Locate and identify every blood parasite.
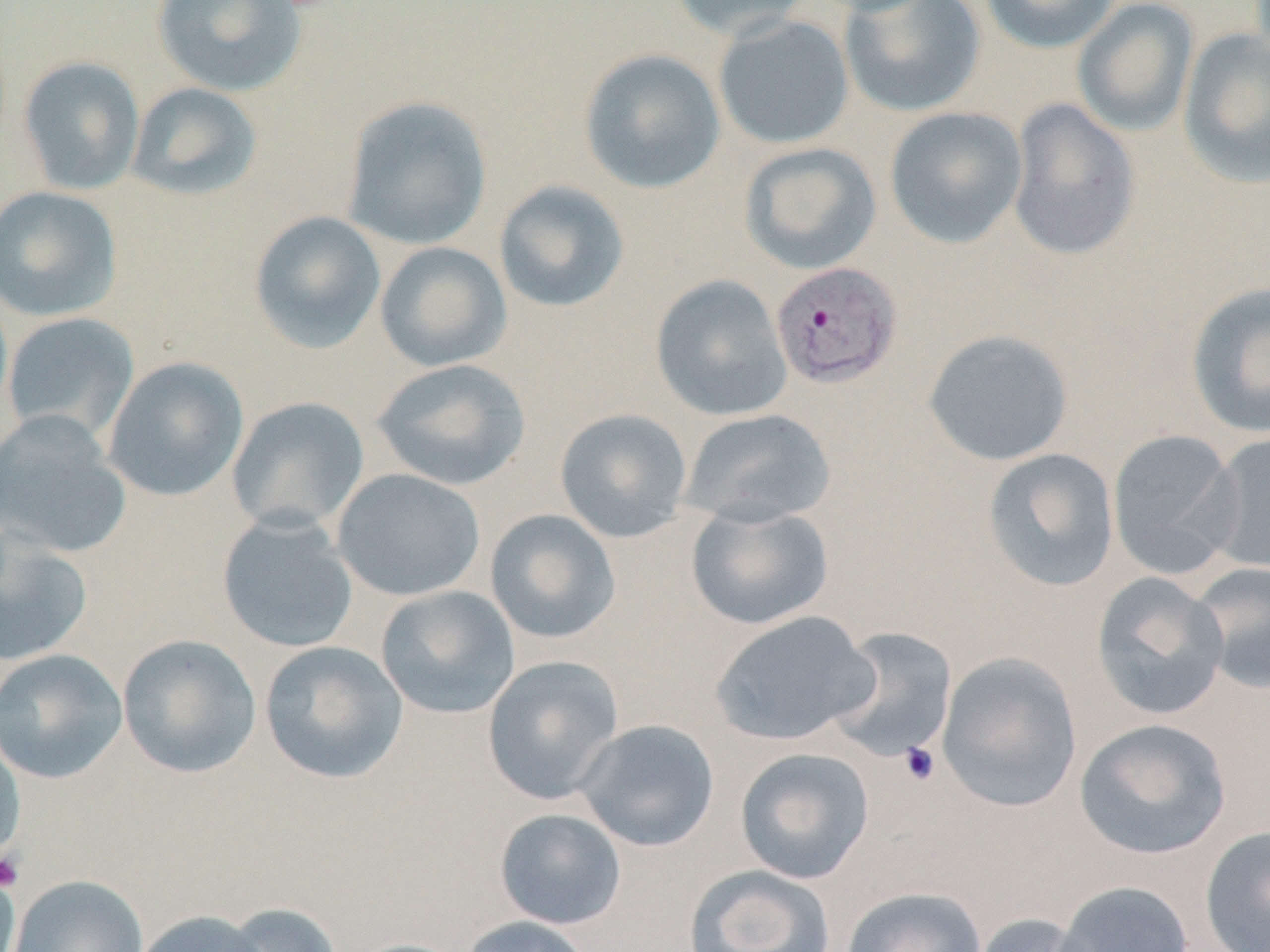

Approximate bounding boxes as (x1, y1, x2, y2) in pixels.
Plasmodium vivax-infected red blood cells: (769, 261, 903, 389).
No Plasmodium falciparum, Plasmodium ovale, Plasmodium malariae, Babesia divergens, or Trypanosoma brucei observed.

Summary:
  - Uninfected red blood cell locations: (151, 0, 307, 98), (667, 0, 817, 41), (839, 0, 987, 118), (978, 0, 1122, 53), (1072, 0, 1200, 137), (713, 15, 855, 150), (1177, 28, 1270, 189), (578, 48, 726, 195), (17, 55, 145, 196), (126, 82, 263, 202), (341, 95, 493, 251), (1006, 97, 1141, 263), (884, 106, 1029, 249), (738, 142, 882, 275), (493, 180, 631, 314), (0, 185, 123, 322), (248, 210, 387, 354), (374, 241, 512, 372), (650, 274, 792, 421), (1185, 281, 1270, 439), (1, 312, 140, 444), (922, 329, 1074, 467), (102, 356, 249, 502), (371, 358, 531, 491), (226, 396, 369, 535), (554, 408, 692, 543), (680, 408, 836, 528), (0, 411, 133, 559), (1106, 428, 1245, 579), (1203, 431, 1270, 575), (981, 448, 1120, 592), (331, 468, 486, 602), (685, 502, 834, 630), (484, 509, 621, 645), (216, 512, 359, 653), (0, 531, 94, 666), (1189, 560, 1270, 696), (1090, 571, 1232, 722), (375, 585, 521, 719), (710, 609, 880, 746), (826, 626, 958, 763), (116, 633, 262, 779), (258, 640, 408, 784), (0, 648, 129, 785), (936, 652, 1083, 813), (482, 655, 625, 805), (1074, 717, 1233, 860), (572, 719, 720, 852), (0, 727, 26, 865), (734, 746, 875, 884), (494, 808, 626, 930), (1199, 824, 1270, 952), (0, 863, 22, 952), (684, 864, 836, 952), (7, 874, 149, 952), (1053, 880, 1195, 952), (841, 886, 988, 952), (219, 902, 345, 952), (129, 909, 271, 952), (971, 912, 1104, 952), (458, 915, 594, 952), (344, 938, 473, 952)
  - Platelet locations: (897, 741, 941, 786), (1, 850, 26, 893)
  - Slide-level diagnosis: Plasmodium vivax
  - Modality: light microscopy
  - Stain: May-Grünwald-Giemsa
  - Preparation: thin blood smear
  - Field of view: one of a larger specimen
  - Magnification: 1000x
  - Image size: 1270×952 pixels